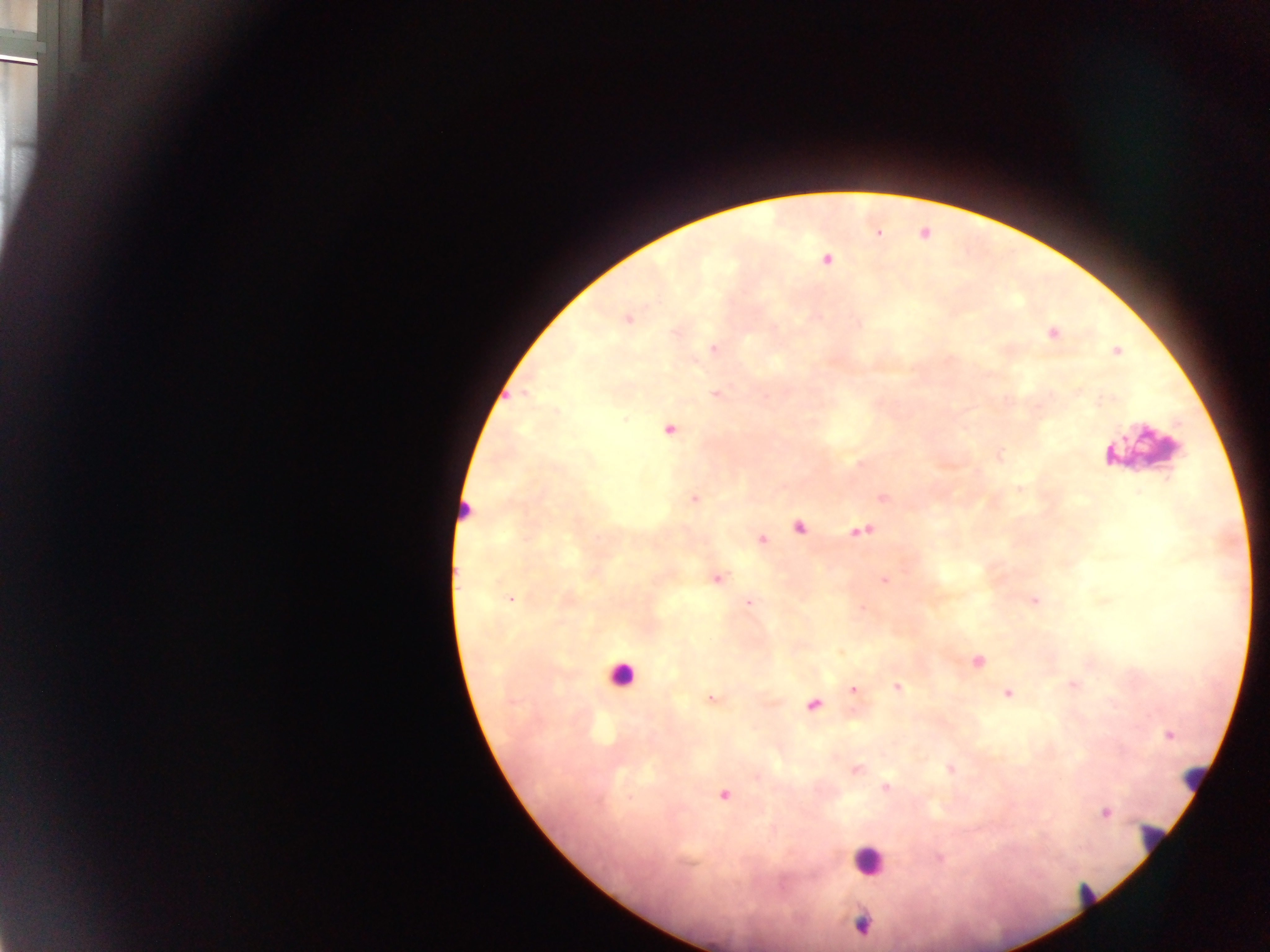

Approximate centers as (x, y) in pixels. Plasmodium parasite locations: (878, 233), (826, 260), (628, 318), (1053, 334), (714, 349), (1117, 350), (716, 394), (669, 430), (694, 499), (799, 527), (860, 531), (762, 539), (718, 579), (885, 579), (510, 600), (1035, 601), (749, 603), (979, 661), (898, 686), (853, 690), (1007, 693), (711, 699), (813, 705), (1169, 734), (950, 769), (857, 770), (886, 786), (724, 795), (1105, 812), (939, 858), (862, 925). Leukocyte locations: (1143, 447), (463, 507), (621, 674), (1191, 778), (1150, 838), (867, 859), (1085, 896). Collected in Ghana. Thick blood smear. Image is 1270×952 pixels. Mobile-phone photograph taken through the microscope. Single field of view.